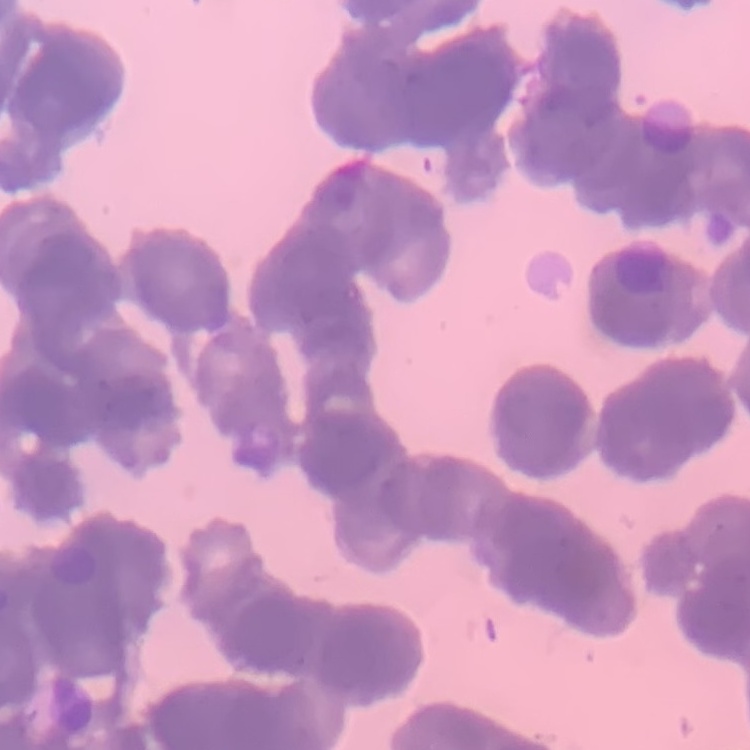

Summary:
  - Erythrocyte morphology: rouleaux formation
  - Preparation: thin blood film
  - Image type: square crop of a larger photomicrograph
  - Stain: Field's or Giemsa